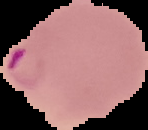

{
  "image_type": "cell region segmented out of the field of view; surrounding area masked to black",
  "result": "malaria parasites identified",
  "preparation": "thin blood smear",
  "image_size": "148×130 pixels"
}